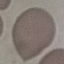
Summary:
  - Malaria status: uninfected
  - Stain: Giemsa
  - Capture: smartphone through the microscope eyepiece
  - Image type: cell patch, automatically extracted from a larger field of view and resized to 64 × 64 pixels
  - Preparation: thin smear